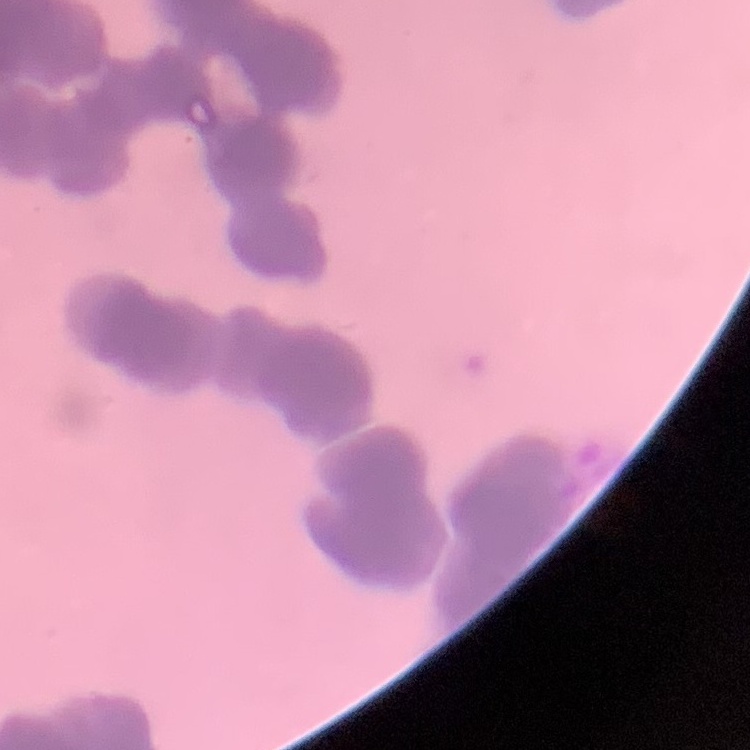 The erythrocytes show rouleaux formation. Thin peripheral smear. One tile cut from a larger photomicrograph. Stained with either Field's or Giemsa.